Assess this cell for malaria.
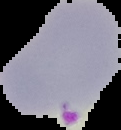
It is parasitized.

image size = 121×130 pixels
image type = segmented cell region with the area outside set to black
preparation = thin blood film